Point out each leukocyte.
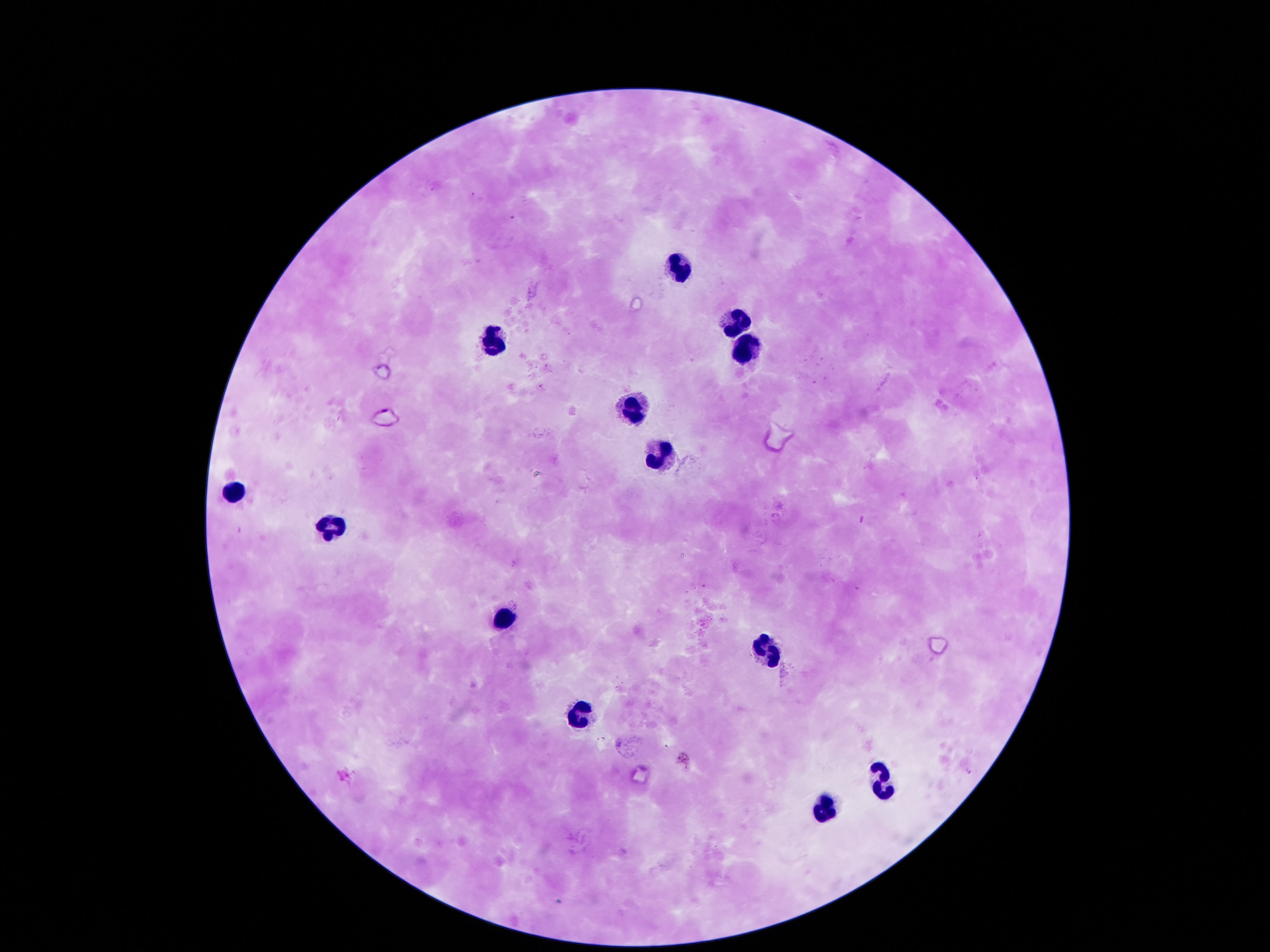

Approximate centers as (x, y) in pixels.
Leukocytes: (681, 262), (732, 320), (490, 338), (742, 345), (632, 403), (658, 449), (235, 490), (332, 523), (503, 613), (768, 648), (577, 714), (887, 778), (823, 804).

{
  "capture": "smartphone camera through the microscope eyepiece",
  "field_of_view": "one from this slide",
  "image_size": "1270×952 pixels",
  "stain": "Giemsa",
  "magnification": "100x",
  "preparation": "thick blood film",
  "patient_malaria_status": "negative"
}